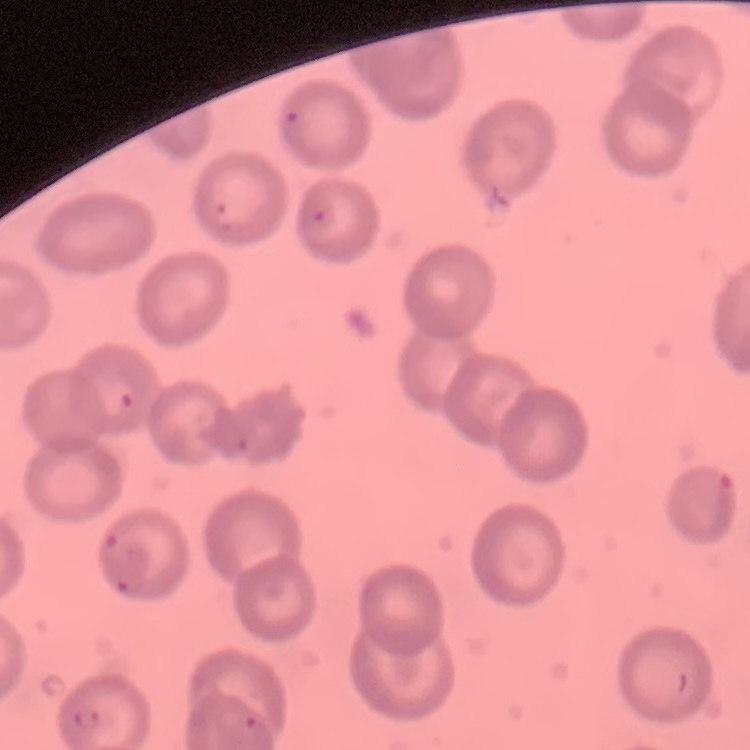

The erythrocytes show no rouleaux formation. Stained with either Field's or Giemsa. One tile cut from a larger photomicrograph. Thin blood smear.